Assess this cell for malaria.
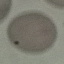

It is uninfected.

Thin blood smear. Giemsa stain. Automatically extracted cell patch, resized to 64 × 64 pixels. Acquired by smartphone through the microscope eyepiece.